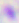
Summary:
  - Modality: photomicrograph
  - Magnification: 400x
  - Identification: Toxoplasma gondii